Assess this cell for malaria.
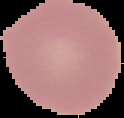

It is uninfected.

Summary:
  - Image size: 124×118 pixels
  - Image type: segmented cell region with the area outside set to black
  - Preparation: thin blood film